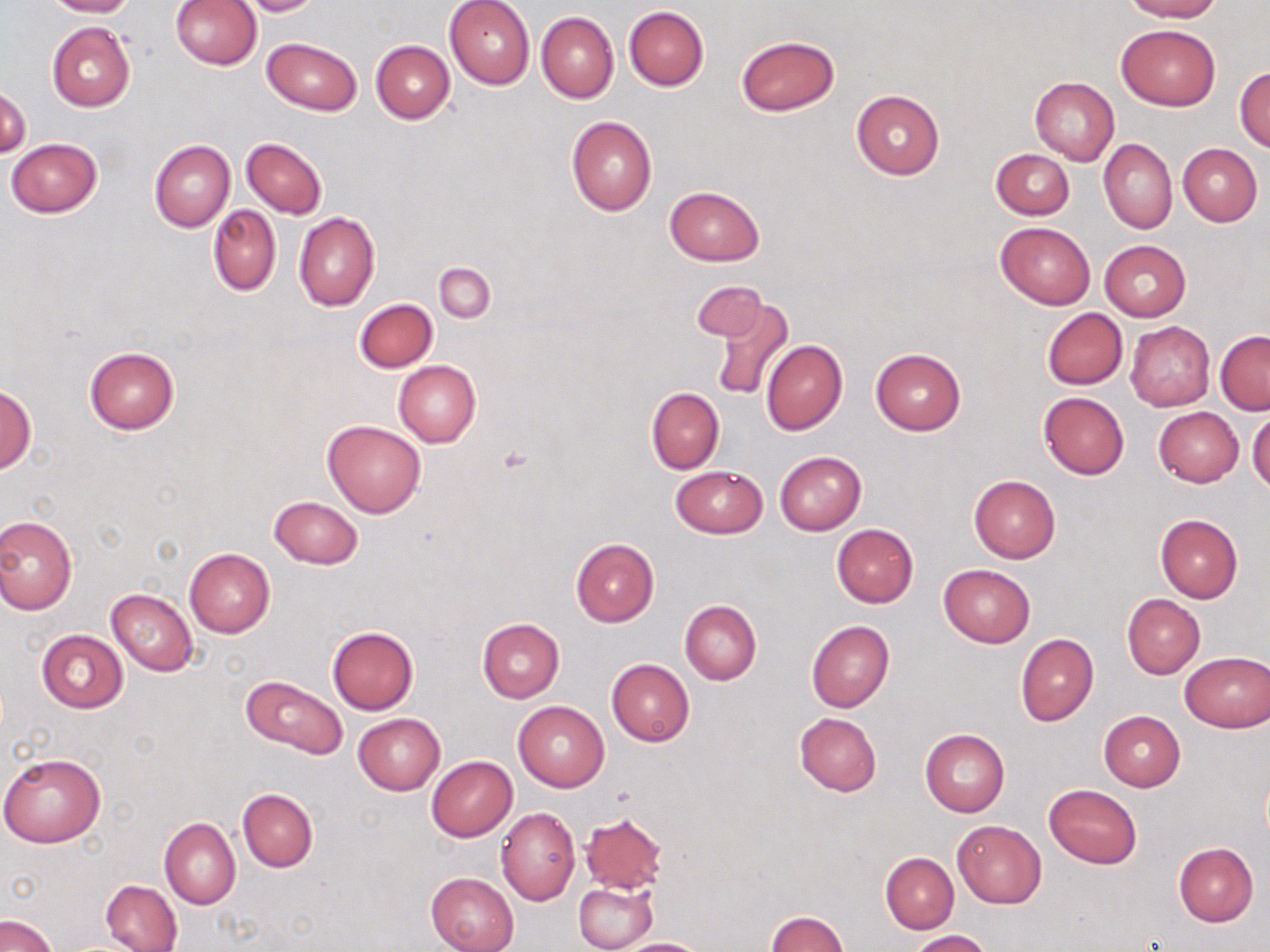
{
  "slide_level_diagnosis": "negative for blood parasites",
  "uninfected_red_blood_cell_locations": "approximate bounding boxes as (x1, y1, x2, y2) in pixels: (44, 0, 135, 18), (170, 0, 261, 71), (236, 0, 323, 15), (444, 0, 536, 90), (1125, 0, 1220, 22), (624, 6, 709, 90), (536, 12, 618, 103), (47, 22, 135, 112), (1116, 23, 1221, 111), (735, 35, 840, 115), (262, 36, 361, 116), (370, 41, 455, 124), (1235, 66, 1270, 152), (1030, 77, 1120, 164), (1, 84, 31, 159), (850, 88, 945, 180), (566, 115, 657, 215), (241, 137, 326, 219), (7, 138, 103, 217), (1098, 139, 1176, 233), (150, 141, 234, 231), (1178, 144, 1261, 226), (991, 149, 1074, 220), (664, 186, 765, 266), (208, 205, 281, 296), (294, 212, 379, 311), (994, 222, 1096, 309), (1100, 240, 1191, 320), (434, 263, 495, 322), (692, 280, 770, 344), (708, 295, 793, 402), (354, 298, 438, 373), (1043, 308, 1127, 389), (1126, 322, 1215, 410), (1216, 331, 1270, 415), (760, 339, 848, 435), (84, 346, 179, 434), (870, 348, 966, 435), (393, 361, 481, 447), (1, 383, 35, 475), (646, 386, 724, 473), (1038, 392, 1129, 479), (1153, 407, 1244, 486), (1247, 409, 1270, 495), (323, 420, 427, 517), (775, 451, 866, 534), (670, 465, 768, 538), (968, 476, 1060, 563), (268, 497, 362, 569), (1154, 513, 1244, 604), (0, 515, 77, 615), (832, 524, 919, 608), (571, 538, 659, 627), (185, 548, 275, 637), (938, 564, 1034, 648), (105, 588, 198, 676), (1122, 594, 1205, 677), (679, 599, 762, 685), (477, 619, 564, 702), (806, 621, 894, 712), (327, 626, 420, 715), (37, 630, 128, 713), (1015, 633, 1098, 727), (1180, 652, 1270, 732), (607, 658, 694, 746), (241, 675, 347, 758), (513, 700, 609, 792), (1098, 712, 1185, 791), (794, 713, 881, 797), (354, 714, 444, 795), (920, 729, 1009, 817), (0, 752, 105, 848), (426, 756, 518, 842), (1045, 784, 1141, 868), (237, 788, 318, 873), (496, 807, 580, 906), (581, 814, 668, 891), (160, 816, 240, 909), (952, 819, 1047, 908), (1173, 843, 1259, 926), (879, 853, 958, 934), (425, 872, 520, 952), (101, 880, 182, 952), (574, 881, 658, 952), (766, 910, 848, 951), (0, 913, 58, 952), (908, 930, 991, 951), (616, 938, 714, 952)",
  "image_size": "1270×952 pixels",
  "stain": "May-Grünwald-Giemsa",
  "field_of_view": "single",
  "magnification": "1000x",
  "preparation": "thin blood film",
  "modality": "optical microscopy"
}